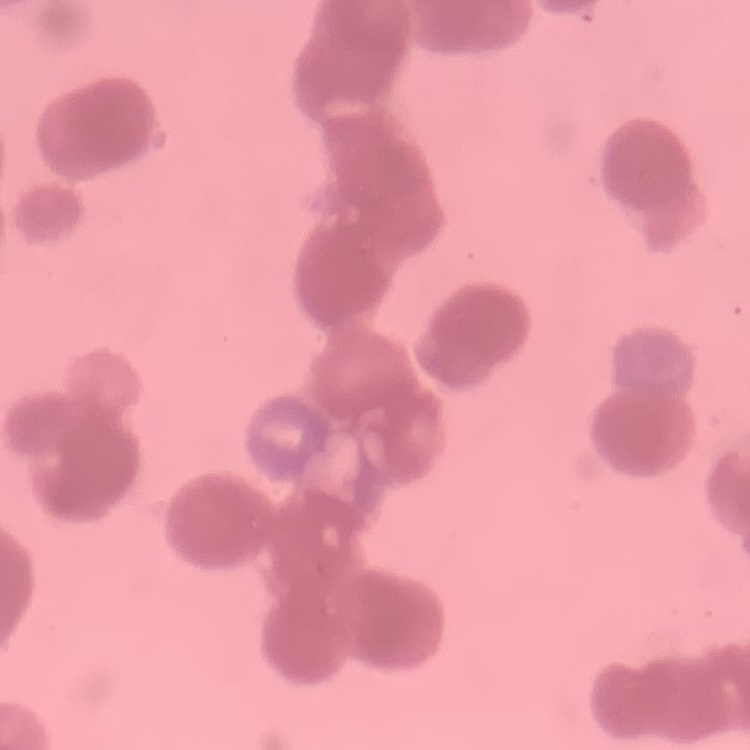 The erythrocytes exhibit rouleaux formation. Field's or Giemsa stain. Square crop of a larger photomicrograph. Thin blood film.